State which cell type is depicted.
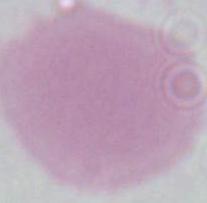
This is an erythrocyte.

{
  "modality": "photomicrograph",
  "magnification": "1000x"
}